Report the malaria status of this cell.
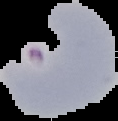

It is parasitized.

Summary:
  - Image type: cell region segmented out of the field of view; surrounding area masked to black
  - Preparation: thin blood smear
  - Image size: 118×121 pixels